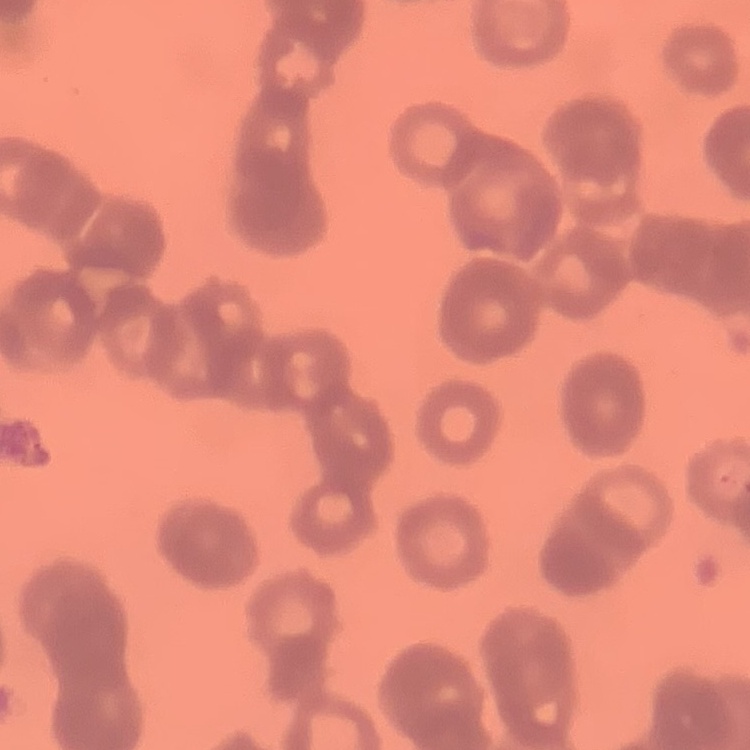

Summary:
  - Red blood cell morphology: rouleaux formation
  - Image type: one tile cut from a larger photomicrograph
  - Preparation: thin peripheral smear
  - Stain: Field's or Giemsa